State which parasite is depicted.
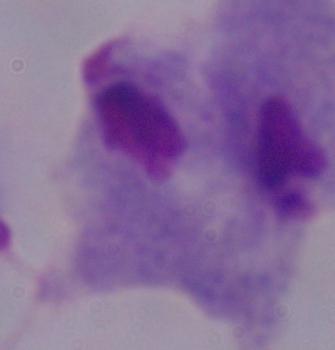

A trichomonad.

Summary:
  - Magnification: 1000x
  - Modality: photomicrograph